Locate every blood parasite and identify its species.
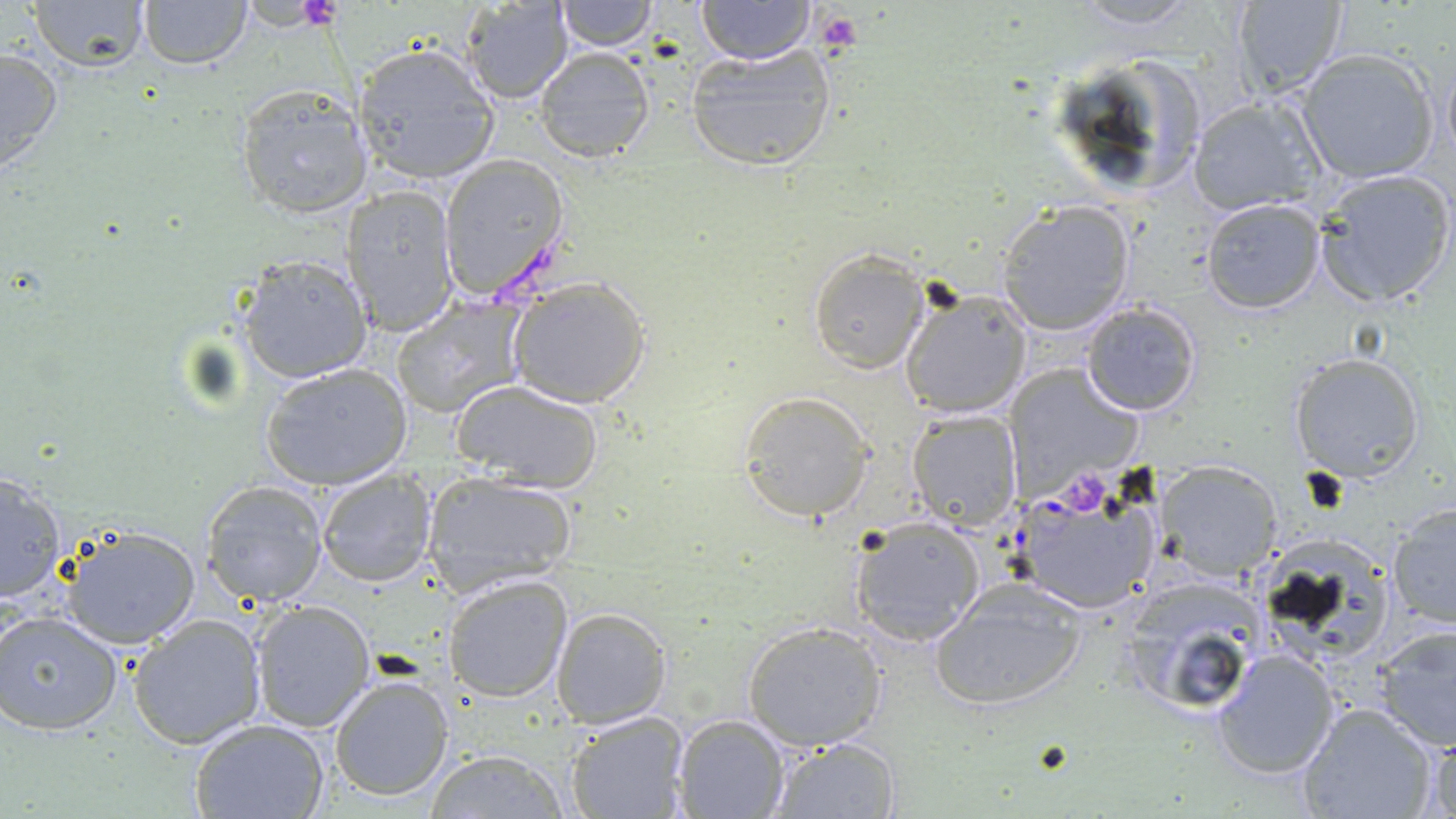

Approximate bounding boxes as (x1,y1)-(x2,y2) corner pairs in pixels.
Plasmodium falciparum-infected red blood cells: (1007,481)-(1162,615).
No Plasmodium ovale, Plasmodium malariae, Plasmodium vivax, Babesia divergens, or Trypanosoma brucei observed.

Uninfected red blood cell locations: (1064,0)-(1209,31), (23,1)-(153,73), (135,1)-(253,69), (461,1)-(575,104), (553,1)-(661,51), (696,1)-(815,66), (1226,1)-(1349,98), (685,41)-(839,172), (349,42)-(502,186), (0,46)-(64,176), (534,46)-(656,162), (1296,48)-(1440,185), (1052,52)-(1211,200), (233,85)-(374,219), (1185,95)-(1325,217), (438,156)-(570,299), (1313,168)-(1454,307), (341,183)-(460,335), (1199,197)-(1325,313), (993,200)-(1137,335), (807,250)-(929,373), (239,255)-(373,384), (509,279)-(653,408), (900,288)-(1031,418), (391,301)-(528,418), (1079,301)-(1202,417), (1288,351)-(1427,482), (260,363)-(414,490), (1002,365)-(1140,492), (454,382)-(604,494), (737,389)-(876,522), (906,410)-(1022,532), (1155,460)-(1283,580), (316,467)-(438,587), (0,470)-(68,602), (421,472)-(575,594), (201,479)-(331,606), (1384,499)-(1456,633), (847,514)-(987,647), (58,525)-(203,648), (441,573)-(571,702), (1117,573)-(1268,721), (930,579)-(1090,710), (250,599)-(375,732), (552,605)-(671,729), (0,609)-(123,737), (127,613)-(267,748), (742,620)-(887,749), (1370,624)-(1456,752), (1212,647)-(1339,778), (1341,651)-(1453,796), (330,672)-(456,802), (1295,703)-(1437,818), (564,711)-(688,818), (672,713)-(790,819), (188,718)-(334,819), (1420,731)-(1456,819), (768,737)-(901,818), (424,746)-(571,818). Platelet locations: (814,10)-(860,53), (1064,478)-(1106,517). Slide-level diagnosis: Plasmodium falciparum. Single field of view. Optical microscopy. May-Grünwald-Giemsa stain. Thin blood smear. Image is 1456×819 pixels. 1000x magnification.